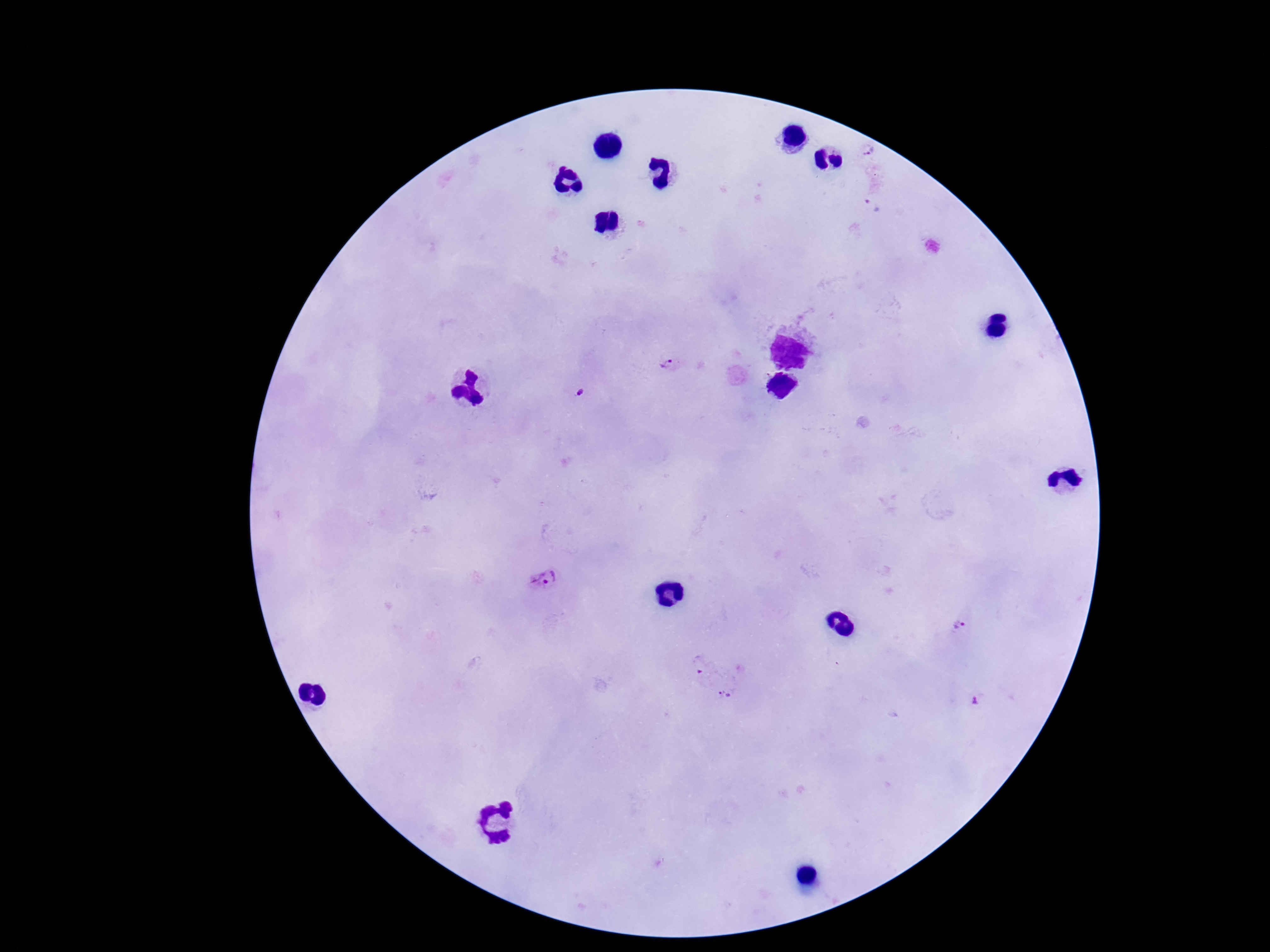
stain = Giemsa
Plasmodium parasite locations = approximate centers as [x, y] in pixels: [868, 152], [871, 205], [668, 367], [581, 391], [544, 579], [960, 627], [725, 694]
image size = 1270×952 pixels
capture = smartphone camera through the microscope eyepiece
field of view = single
preparation = thick blood film
patient malaria status = infected
magnification = 100x